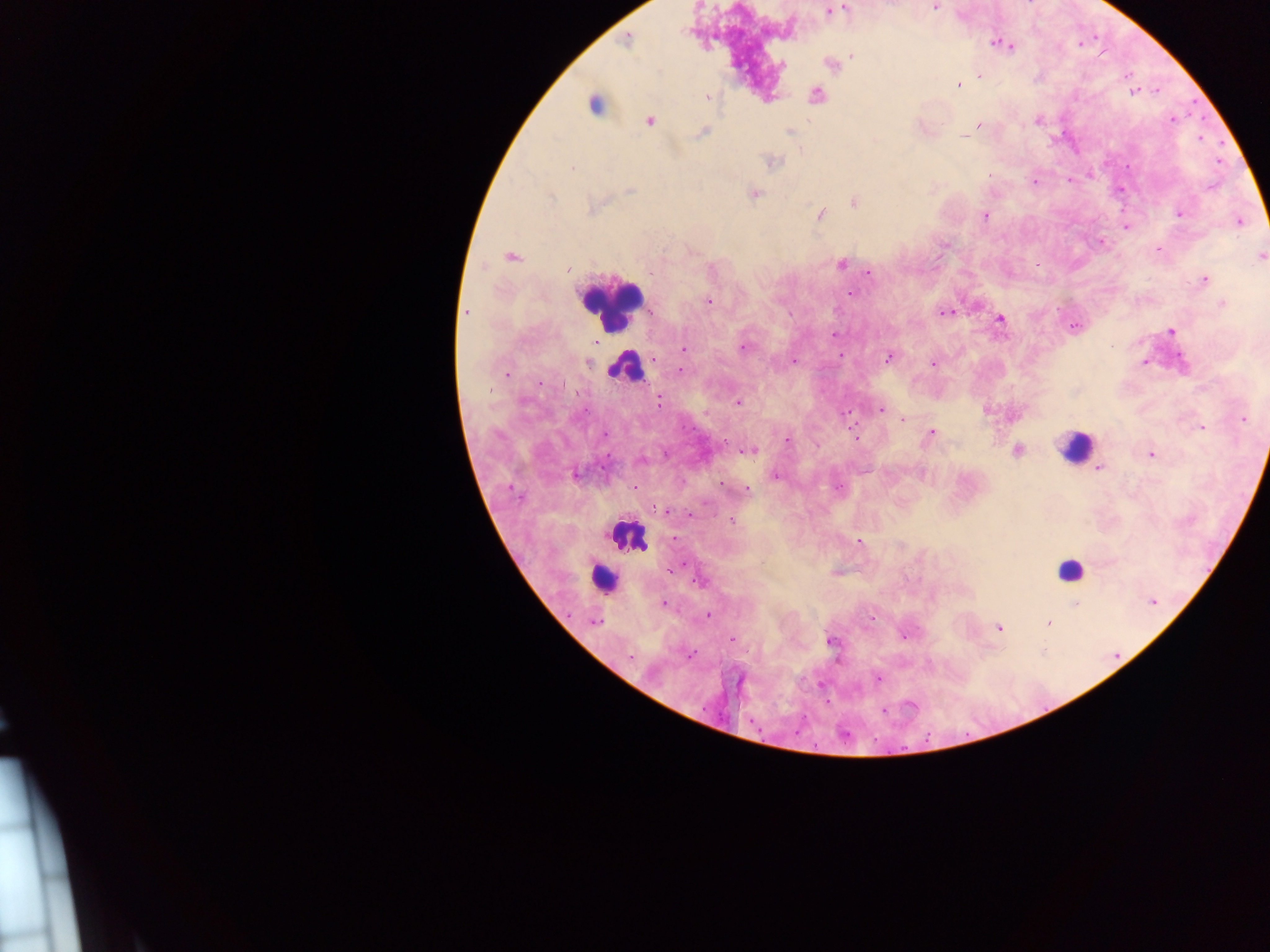

preparation = thick blood smear
country = Ghana
capture = mobile-phone photograph through a microscope
Plasmodium parasite locations = approximate centers as {x, y} in pixels: {934, 7}, {845, 8}, {828, 11}, {627, 40}, {999, 43}, {1007, 45}, {852, 55}, {782, 65}, {832, 66}, {979, 75}, {958, 85}, {1133, 92}, {816, 95}, {707, 96}, {593, 105}, {1172, 119}, {650, 121}, {1037, 121}, {978, 125}, {701, 132}, {789, 132}, {964, 136}, {772, 162}, {572, 167}, {1068, 180}, {1034, 182}, {629, 190}, {754, 193}, {550, 197}, {854, 202}, {592, 208}, {820, 214}, {1179, 214}, {985, 216}, {1241, 221}, {1125, 228}, {1158, 249}, {1261, 256}, {511, 257}, {842, 263}, {1037, 264}, {567, 270}, {870, 274}, {1204, 279}, {850, 294}, {709, 302}, {1222, 304}, {466, 312}, {945, 313}, {999, 319}, {1171, 331}, {835, 334}, {683, 348}, {743, 348}, {840, 355}, {888, 357}, {793, 360}, {1144, 363}, {588, 364}, {933, 364}, {681, 371}, {507, 373}, {658, 401}, {738, 403}, {880, 410}, {846, 413}, {1243, 419}, {904, 420}, {1201, 428}, {606, 432}, {932, 433}, {855, 437}, {787, 440}, {750, 451}, {1018, 451}, {1150, 454}, {641, 459}, {1099, 467}, {575, 475}, {776, 476}, {746, 489}, {663, 510}, {732, 521}, {859, 542}, {672, 569}, {701, 581}, {1153, 602}, {664, 604}, {1075, 604}, {708, 616}, {594, 622}, {1049, 623}, {998, 627}, {904, 636}, {732, 640}, {831, 641}, {689, 656}, {877, 679}
leukocyte locations = approximate centers as {x, y} in pixels: {610, 304}, {626, 365}, {1075, 447}, {625, 537}, {1069, 569}, {604, 578}
field of view = single
image size = 1270×952 pixels